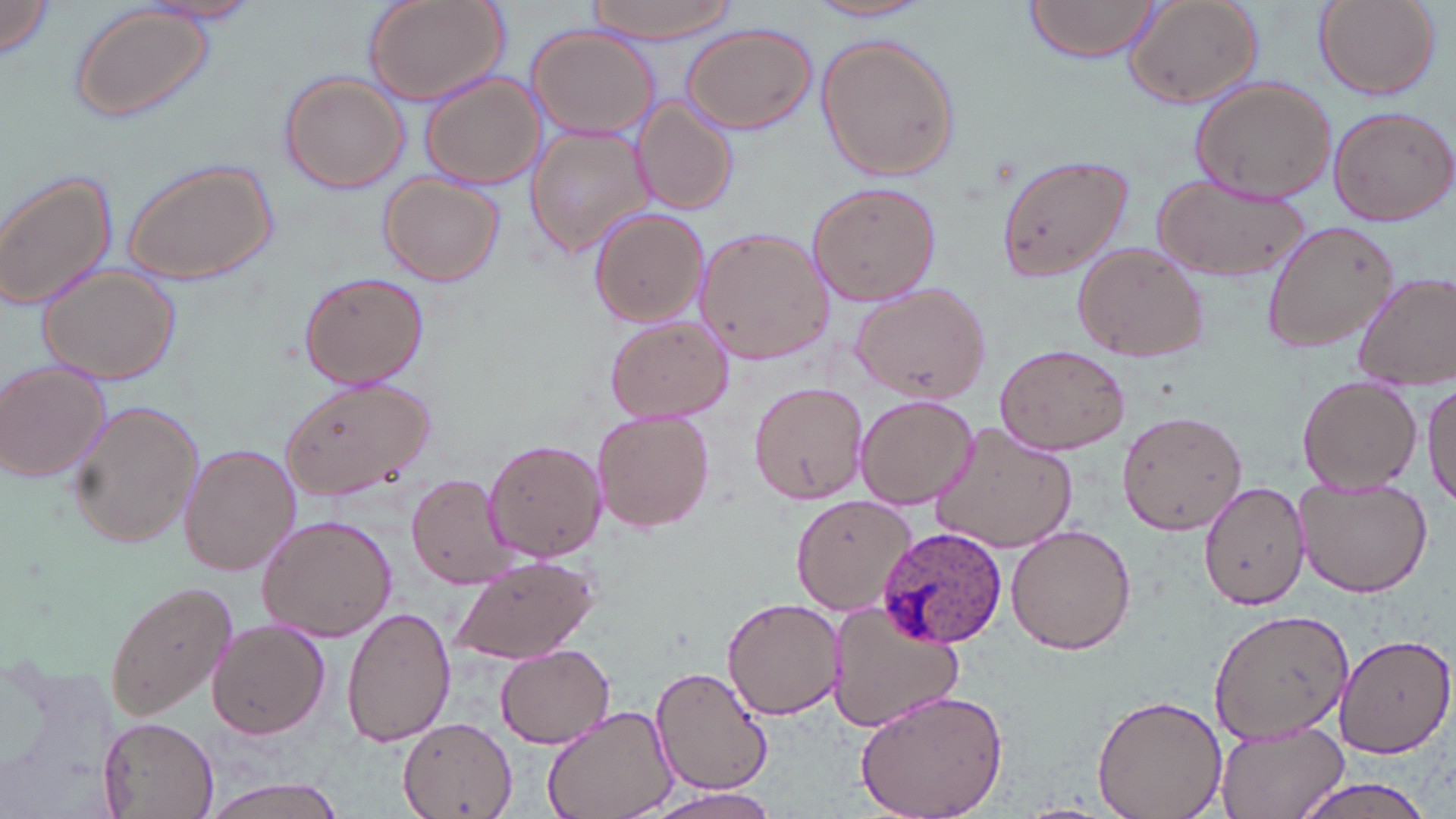
Summary:
  - Coordinate format: approximate bounding boxes as [x1, y1, x2, y2] in pixels
  - Uninfected red blood cell locations: [0, 0, 58, 62], [143, 0, 263, 28], [362, 0, 511, 109], [587, 0, 742, 43], [1021, 0, 1165, 62], [1121, 0, 1264, 109], [1313, 0, 1439, 98], [809, 1, 933, 24], [68, 2, 216, 123], [681, 24, 817, 134], [527, 26, 660, 139], [816, 32, 960, 183], [279, 71, 408, 194], [419, 71, 546, 189], [1190, 77, 1333, 205], [632, 98, 739, 219], [1327, 105, 1455, 225], [524, 125, 655, 258], [994, 150, 1133, 282], [120, 159, 278, 285], [0, 170, 122, 312], [378, 174, 505, 287], [1151, 174, 1311, 284], [805, 179, 942, 307], [589, 207, 709, 327], [1262, 218, 1400, 355], [693, 227, 834, 366], [1070, 241, 1209, 363], [39, 265, 180, 387], [299, 270, 428, 390], [1356, 272, 1456, 390], [849, 282, 990, 403], [603, 317, 732, 423], [994, 342, 1131, 455], [0, 361, 111, 484], [275, 374, 435, 503], [1297, 374, 1421, 493], [748, 378, 869, 504], [1423, 380, 1456, 504], [854, 395, 979, 509], [67, 399, 205, 550], [592, 408, 716, 535], [1117, 408, 1247, 537], [930, 422, 1079, 555], [484, 439, 607, 561], [181, 443, 300, 576], [406, 473, 524, 589], [1201, 481, 1313, 611], [1294, 485, 1433, 598], [792, 494, 914, 613], [257, 515, 397, 642], [1006, 523, 1136, 655], [448, 552, 600, 666], [105, 580, 240, 721], [721, 597, 844, 719], [827, 602, 965, 733], [342, 604, 457, 747], [1207, 606, 1354, 746], [207, 620, 330, 741], [1333, 632, 1455, 756], [495, 644, 615, 748], [651, 665, 774, 795], [852, 687, 1010, 819], [1091, 692, 1228, 819], [543, 704, 677, 819], [97, 716, 218, 819], [396, 717, 519, 819], [1211, 717, 1351, 819], [1281, 775, 1443, 819], [204, 779, 347, 817], [642, 788, 781, 819]
  - Plasmodium ovale-infected red blood cell locations: [874, 524, 1006, 647]
  - Slide-level diagnosis: Plasmodium ovale
  - Modality: light microscopy
  - Field of view: one of a larger specimen
  - Magnification: 1000x
  - Image size: 1456×819 pixels
  - Stain: May-Grünwald-Giemsa
  - Preparation: thin blood film